Report the malaria status of this cell.
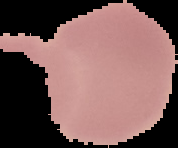
It is uninfected.

preparation = thin blood film
image type = segmented cell region on a black background
image size = 178×148 pixels